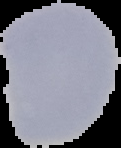

Summary:
  - Preparation: thin blood smear
  - Image type: cell region segmented out of the field of view; surrounding area masked to black
  - Image size: 121×148 pixels
  - Result: negative for malaria parasites